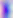
modality = micrograph
magnification = 400x
identification = Toxoplasma gondii